Report the malaria status of this cell.
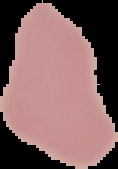
It is uninfected.

preparation = thin blood film
image type = cell region segmented out of the field of view; surrounding area masked to black
image size = 118×169 pixels